Assess for malaria.
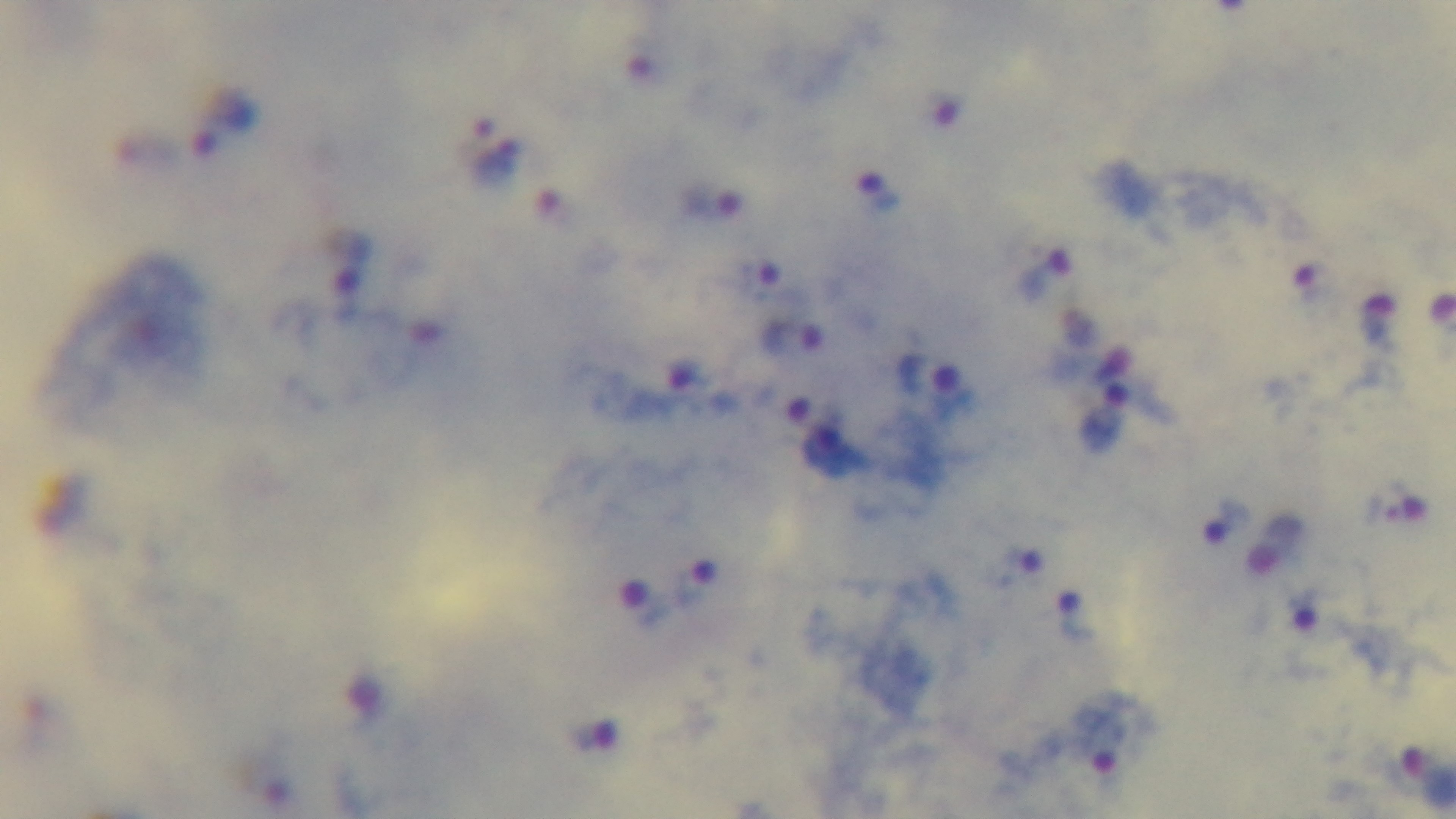
Positive.

{
  "preparation": "thick smear",
  "capture": "mounted 4K digital camera",
  "modality": "light microscopy",
  "stain": "Giemsa",
  "field_of_view": "one from the slide",
  "objective": "100x oil immersion"
}